Identify the parasite.
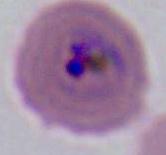

This is Plasmodium.

modality = micrograph
magnification = 400x or 1000x